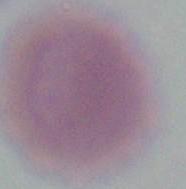
identification: red blood cell
modality: micrograph
magnification: 1000x